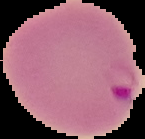
Image is 145×139 pixels. Result: Plasmodium parasites identified. From a thin blood film. The area outside the segmented cell region is set to black.